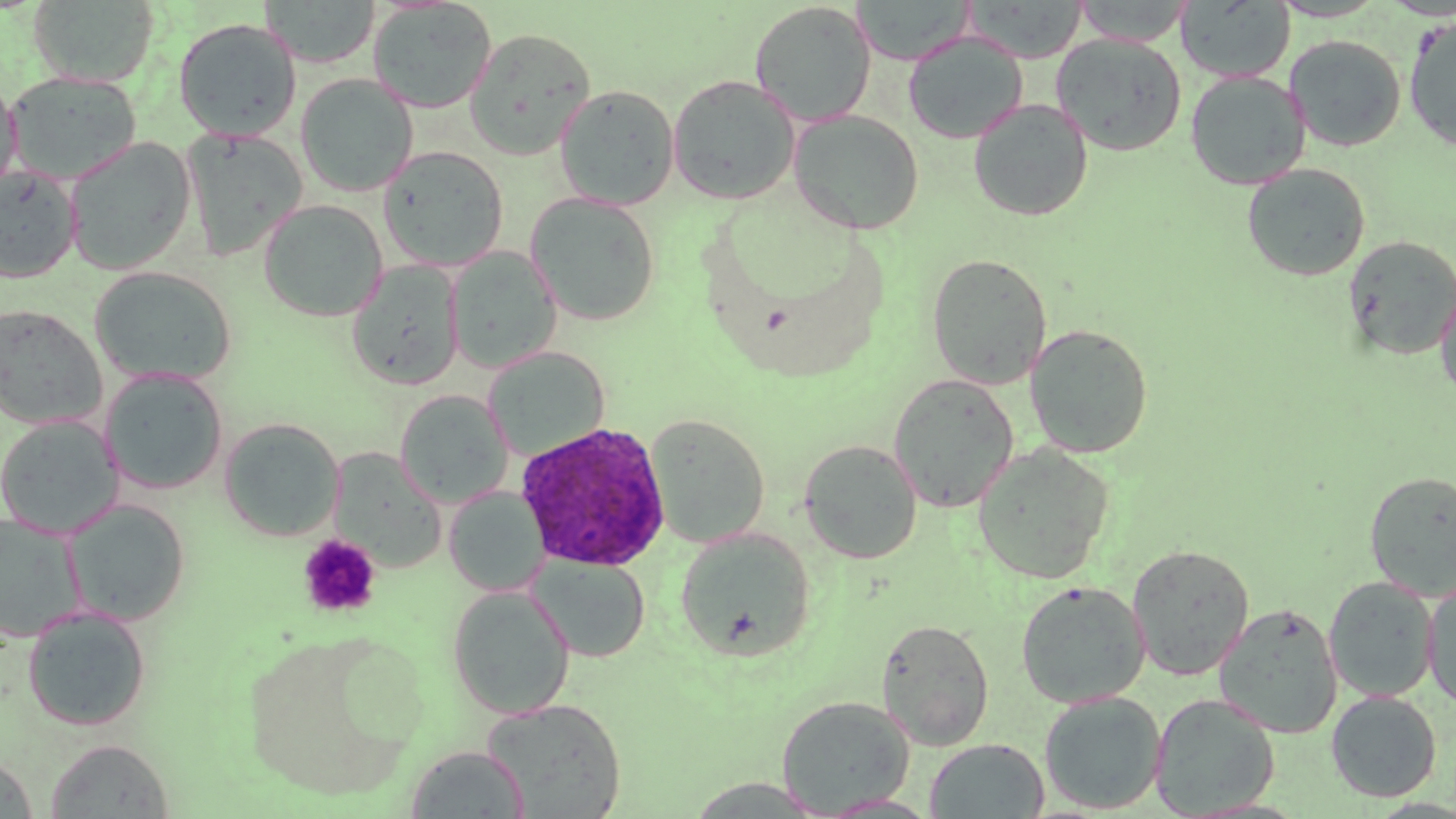
Summary:
  - Coordinate format: approximate bounding boxes as named x1/y1/x2/y2 corners in pixels
  - Uninfected red blood cell locations: (x1=29, y1=0, x2=160, y2=87), (x1=259, y1=0, x2=381, y2=68), (x1=851, y1=0, x2=976, y2=65), (x1=963, y1=0, x2=1087, y2=62), (x1=1177, y1=0, x2=1295, y2=82), (x1=367, y1=1, x2=498, y2=114), (x1=1073, y1=1, x2=1193, y2=45), (x1=749, y1=2, x2=877, y2=127), (x1=1403, y1=14, x2=1456, y2=151), (x1=173, y1=17, x2=302, y2=141), (x1=464, y1=27, x2=596, y2=160), (x1=903, y1=31, x2=1028, y2=144), (x1=1051, y1=34, x2=1188, y2=156), (x1=1284, y1=35, x2=1406, y2=152), (x1=6, y1=70, x2=142, y2=185), (x1=1185, y1=70, x2=1310, y2=190), (x1=0, y1=73, x2=21, y2=200), (x1=296, y1=73, x2=418, y2=197), (x1=667, y1=74, x2=801, y2=205), (x1=555, y1=84, x2=680, y2=210), (x1=969, y1=99, x2=1093, y2=222), (x1=789, y1=110, x2=924, y2=235), (x1=182, y1=127, x2=308, y2=262), (x1=63, y1=137, x2=196, y2=275), (x1=378, y1=146, x2=509, y2=272), (x1=1241, y1=163, x2=1371, y2=281), (x1=0, y1=165, x2=82, y2=284), (x1=525, y1=192, x2=661, y2=326), (x1=257, y1=199, x2=388, y2=322), (x1=1343, y1=235, x2=1456, y2=360), (x1=446, y1=247, x2=562, y2=373), (x1=925, y1=252, x2=1052, y2=389), (x1=346, y1=260, x2=465, y2=391), (x1=89, y1=267, x2=237, y2=387), (x1=1435, y1=277, x2=1456, y2=403), (x1=0, y1=305, x2=107, y2=429), (x1=1024, y1=323, x2=1154, y2=458), (x1=483, y1=346, x2=610, y2=461), (x1=99, y1=368, x2=229, y2=495), (x1=888, y1=373, x2=1020, y2=513), (x1=394, y1=389, x2=513, y2=508), (x1=644, y1=413, x2=770, y2=548), (x1=0, y1=415, x2=123, y2=538), (x1=219, y1=418, x2=344, y2=541), (x1=799, y1=439, x2=922, y2=564), (x1=971, y1=444, x2=1115, y2=584), (x1=329, y1=448, x2=447, y2=573), (x1=1364, y1=471, x2=1456, y2=600), (x1=443, y1=487, x2=549, y2=598), (x1=64, y1=499, x2=191, y2=627), (x1=0, y1=514, x2=85, y2=643), (x1=675, y1=527, x2=816, y2=662), (x1=1126, y1=544, x2=1255, y2=681), (x1=529, y1=555, x2=650, y2=663), (x1=1323, y1=576, x2=1439, y2=702), (x1=1423, y1=578, x2=1456, y2=711), (x1=1016, y1=580, x2=1150, y2=708), (x1=447, y1=585, x2=575, y2=719), (x1=1214, y1=603, x2=1343, y2=738), (x1=22, y1=606, x2=151, y2=731), (x1=876, y1=617, x2=995, y2=750), (x1=240, y1=631, x2=423, y2=799), (x1=1326, y1=690, x2=1442, y2=802), (x1=1039, y1=691, x2=1167, y2=814), (x1=1149, y1=693, x2=1280, y2=817), (x1=776, y1=695, x2=915, y2=816), (x1=482, y1=697, x2=626, y2=817), (x1=45, y1=738, x2=174, y2=818), (x1=925, y1=738, x2=1049, y2=818), (x1=405, y1=745, x2=530, y2=818), (x1=0, y1=753, x2=38, y2=818), (x1=817, y1=794, x2=942, y2=818)
  - Platelet locations: (x1=297, y1=534, x2=381, y2=618)
  - Plasmodium ovale-infected red blood cell locations: (x1=516, y1=420, x2=671, y2=571)
  - Slide-level diagnosis: Plasmodium ovale
  - Modality: light microscopy
  - Stain: May-Grünwald-Giemsa
  - Image size: 1456×819 pixels
  - Magnification: 1000x
  - Preparation: thin blood smear
  - Field of view: single